Report the malaria status of this cell.
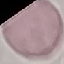
Uninfected.

Acquired by smartphone through the microscope eyepiece. Automatically extracted cell patch, resized to 64 × 64 pixels. Giemsa-stained preparation. Thin smear of blood.